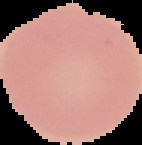
image size = 142×145 pixels
preparation = thin blood film
image type = segmented cell region on a black background
malaria status = uninfected